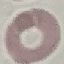
{
  "result": "no malaria parasites detected",
  "stain": "Giemsa",
  "capture": "smartphone through the microscope eyepiece",
  "image_type": "automatically extracted cell patch, resized to 64 × 64 pixels",
  "preparation": "thin blood film"
}